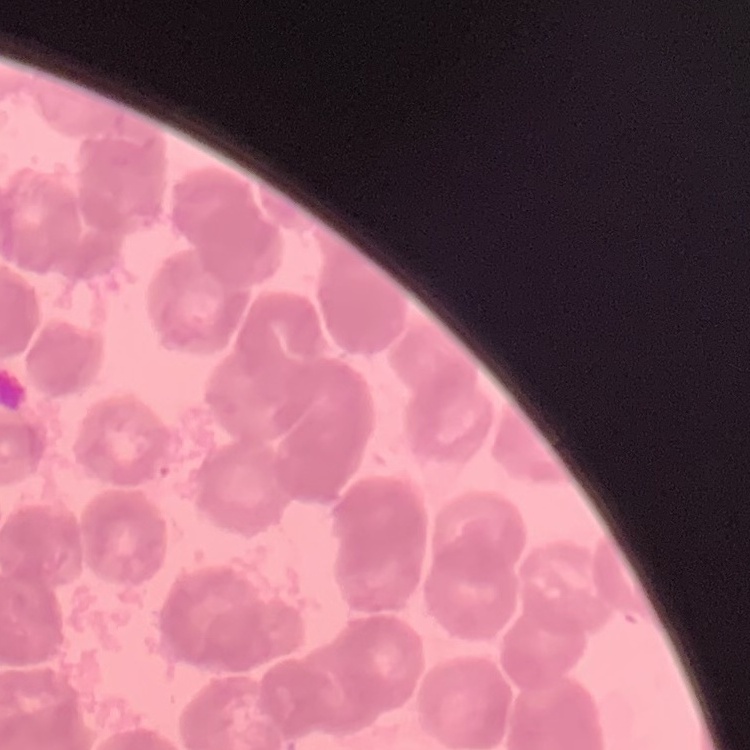

Summary:
  - Red blood cell morphology: rouleaux formation
  - Stain: Field's or Giemsa
  - Image type: one tile cut from a larger photomicrograph
  - Preparation: thin blood film